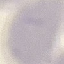
Summary:
  - Result: no malaria parasites seen
  - Preparation: thin smear
  - Image type: automatically extracted cell patch, resized to 64 × 64 pixels
  - Capture: smartphone camera at the microscope eyepiece
  - Stain: Giemsa